Report the malaria status of this cell.
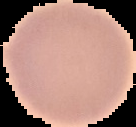
Uninfected.

Cell region segmented out of the field of view; the surrounding area is masked to black. Image is 136×127 pixels. From a thin blood film.